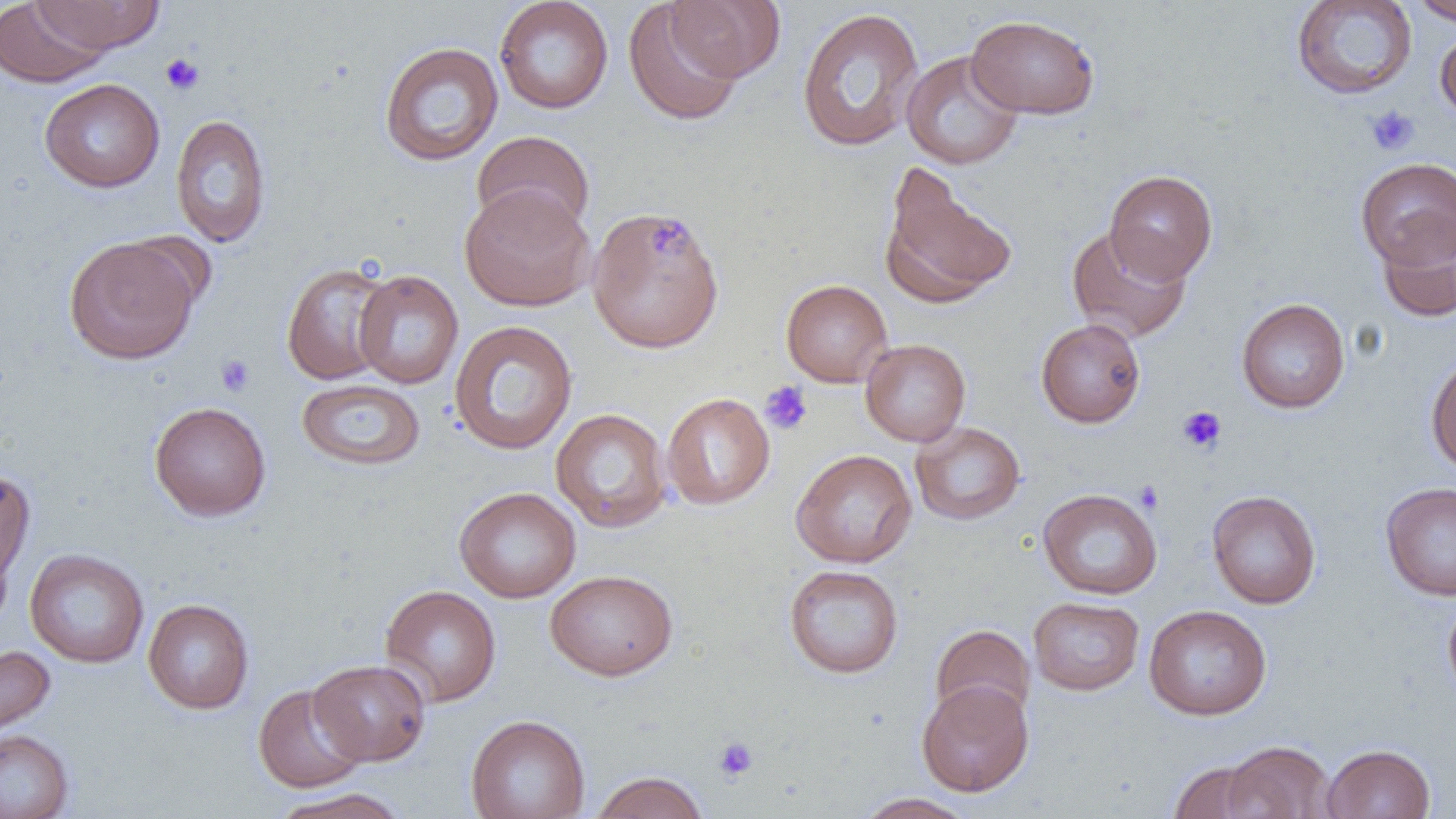
Approximate bounding boxes as (x1,y1)-(x2,y2) corner pairs in pixels. Uninfected red blood cell locations: (0,0)-(110,87), (30,0)-(165,54), (494,0)-(614,114), (667,0)-(785,83), (1290,0)-(1418,100), (1411,0)-(1456,25), (623,2)-(745,126), (795,7)-(924,152), (966,15)-(1100,119), (1435,27)-(1456,124), (379,41)-(504,166), (900,50)-(1024,169), (39,78)-(165,193), (170,113)-(271,247), (471,130)-(595,237), (1355,157)-(1456,268), (879,166)-(1017,308), (1105,169)-(1218,283), (459,184)-(595,311), (590,211)-(724,349), (1378,214)-(1456,323), (1067,226)-(1192,343), (64,235)-(200,364), (281,262)-(396,385), (353,270)-(464,389), (780,278)-(893,387), (1236,298)-(1350,414), (1036,318)-(1145,427), (449,320)-(577,455), (860,338)-(971,447), (1425,351)-(1456,474), (296,378)-(426,471), (661,393)-(775,510), (149,401)-(271,521), (550,408)-(672,532), (910,421)-(1026,526), (790,449)-(917,568), (0,469)-(35,593), (1380,481)-(1456,601), (454,486)-(581,603), (1037,488)-(1162,599), (1206,490)-(1321,608), (25,549)-(149,668), (784,564)-(904,678), (546,569)-(677,680), (379,585)-(502,707), (1442,594)-(1456,704), (1028,596)-(1144,695), (142,598)-(254,714), (1144,605)-(1272,720), (930,624)-(1035,726), (0,644)-(56,741), (309,659)-(431,765), (916,679)-(1034,796), (252,683)-(369,793), (466,714)-(590,819), (0,729)-(75,818), (1219,740)-(1335,819), (1322,743)-(1435,819), (1169,761)-(1269,819), (590,771)-(710,819), (267,787)-(411,819), (854,792)-(977,819). Platelet locations: (159,53)-(205,95), (1366,105)-(1419,156), (646,216)-(696,259), (216,354)-(255,397), (759,380)-(813,435), (1177,405)-(1227,453), (1134,480)-(1164,515), (713,736)-(759,782). Slide-level diagnosis: no evidence of blood parasites. Thin blood film. Single field of view. Image is 1456×819 pixels. Optical microscopy. 1000x magnification.